Identify the parasite.
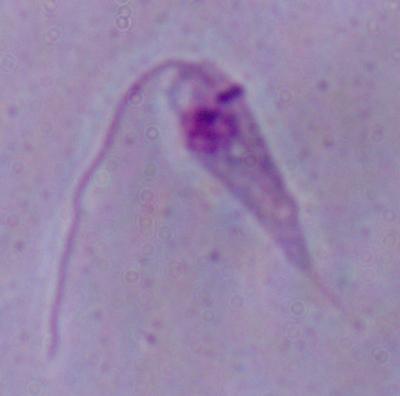

Leishmania.

Summary:
  - Modality: micrograph
  - Magnification: 1000x